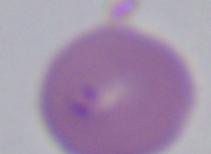

modality = photomicrograph
magnification = 1000x
identification = Babesia